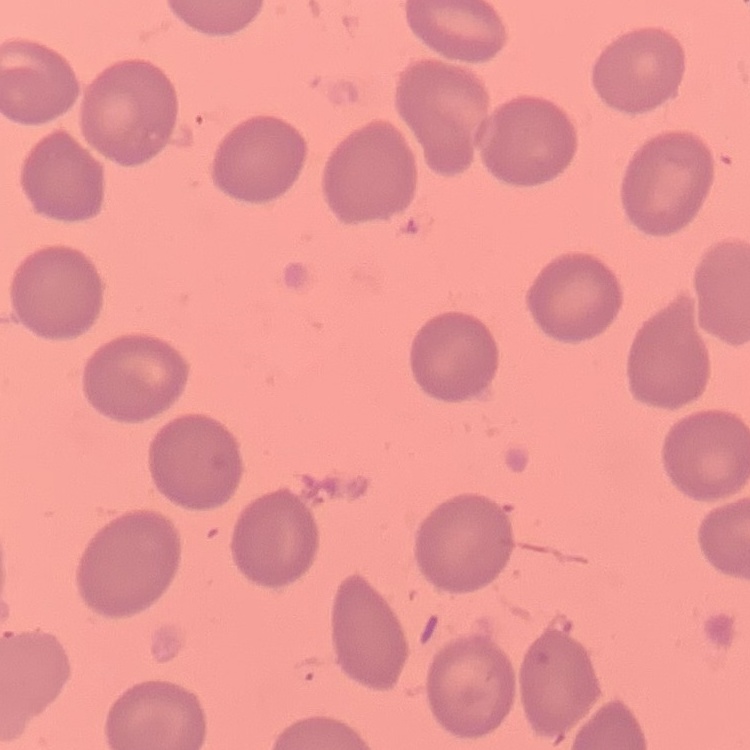
Summary:
  - Erythrocyte morphology: no rouleaux formation
  - Stain: Field's or Giemsa
  - Image type: one tile cut from a larger photomicrograph
  - Preparation: thin peripheral smear